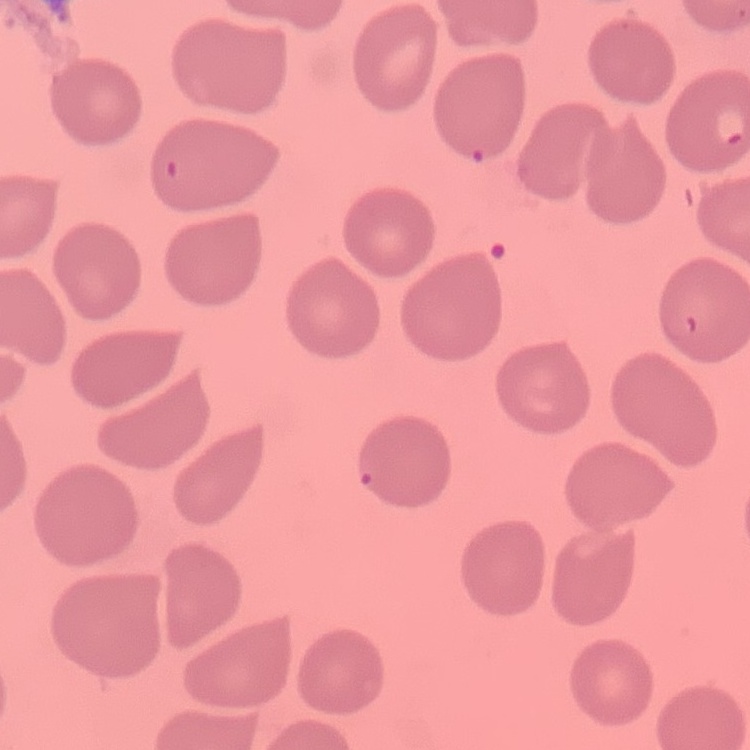

Summary:
  - Red blood cell morphology: no rouleaux formation
  - Image type: square crop of a larger photomicrograph
  - Preparation: thin blood smear
  - Stain: Field's or Giemsa